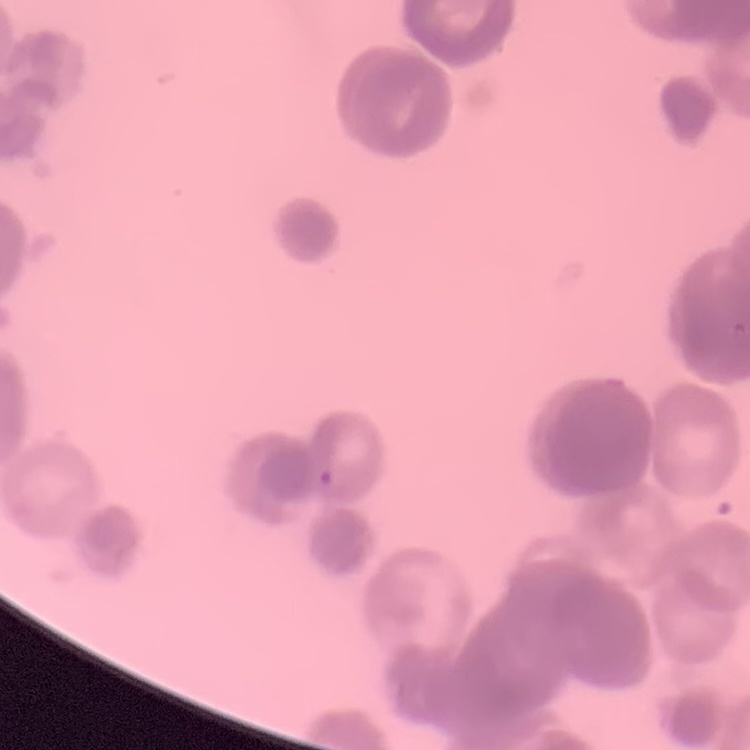

{
  "erythrocyte_morphology": "rouleaux formation",
  "stain": "Field's or Giemsa",
  "image_type": "one tile cut from a larger photomicrograph",
  "preparation": "thin blood film"
}